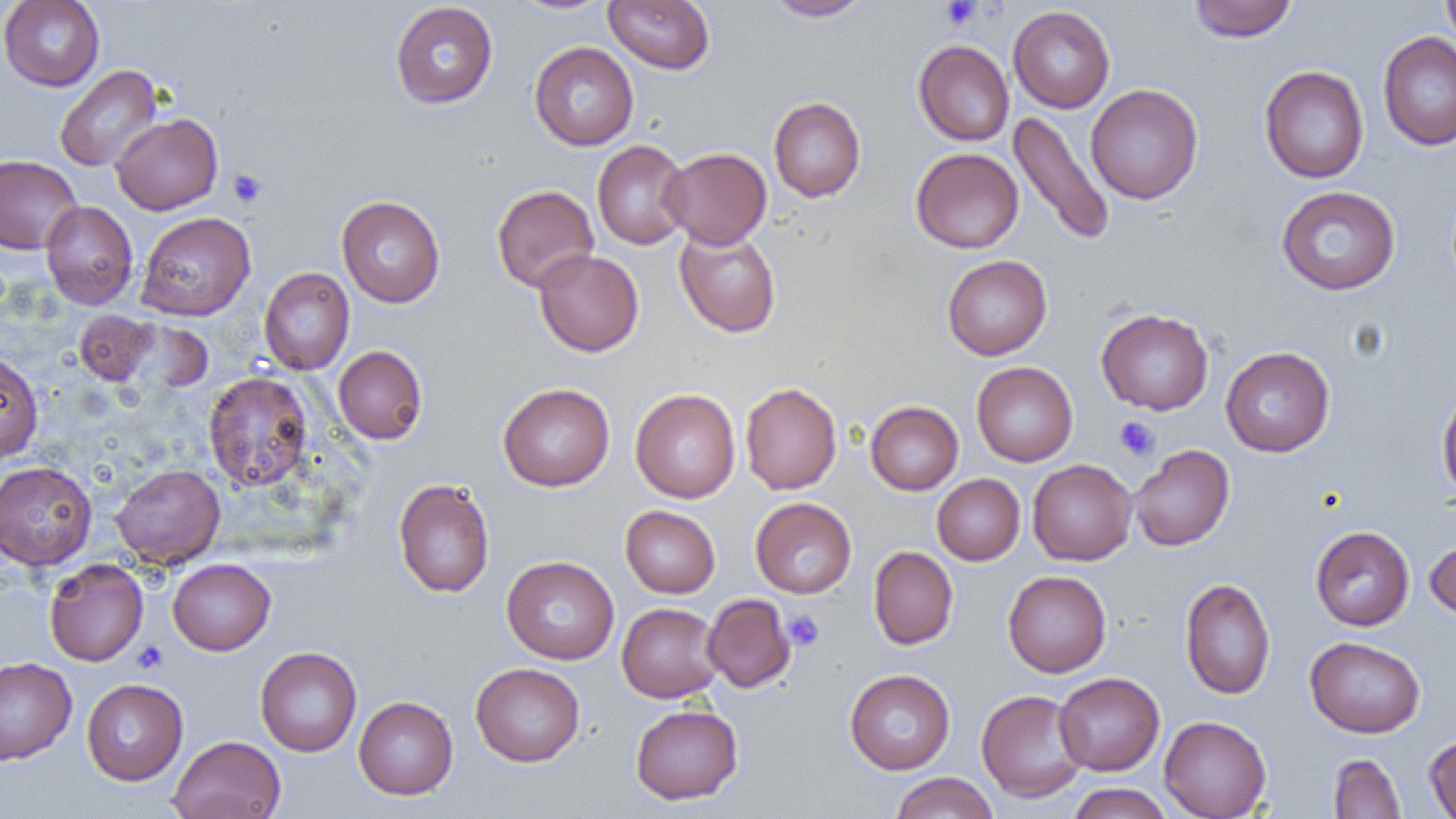

{
  "slide_level_diagnosis": "negative for blood parasites",
  "platelet_locations": "approximate bounding boxes as named x1/y1/x2/y2 corners in pixels: (x1=940, y1=0, x2=981, y2=29), (x1=228, y1=169, x2=267, y2=210), (x1=1114, y1=416, x2=1160, y2=461), (x1=783, y1=610, x2=824, y2=651), (x1=132, y1=641, x2=168, y2=673)",
  "field_of_view": "single",
  "uninfected_red_blood_cell_locations": "approximate bounding boxes as named x1/y1/x2/y2 corners in pixels: (x1=0, y1=0, x2=105, y2=91), (x1=509, y1=0, x2=616, y2=15), (x1=603, y1=0, x2=715, y2=74), (x1=764, y1=0, x2=873, y2=21), (x1=1188, y1=0, x2=1297, y2=42), (x1=1441, y1=0, x2=1456, y2=52), (x1=389, y1=2, x2=498, y2=108), (x1=1008, y1=6, x2=1115, y2=113), (x1=1378, y1=31, x2=1456, y2=150), (x1=913, y1=40, x2=1014, y2=146), (x1=529, y1=41, x2=639, y2=150), (x1=54, y1=65, x2=162, y2=172), (x1=1260, y1=65, x2=1369, y2=183), (x1=1085, y1=84, x2=1203, y2=204), (x1=769, y1=96, x2=865, y2=202), (x1=1008, y1=111, x2=1116, y2=247), (x1=111, y1=113, x2=222, y2=215), (x1=592, y1=140, x2=692, y2=250), (x1=661, y1=147, x2=772, y2=249), (x1=911, y1=148, x2=1024, y2=253), (x1=0, y1=154, x2=83, y2=254), (x1=492, y1=184, x2=599, y2=293), (x1=1276, y1=186, x2=1400, y2=295), (x1=336, y1=195, x2=446, y2=307), (x1=40, y1=201, x2=138, y2=309), (x1=135, y1=212, x2=256, y2=321), (x1=674, y1=225, x2=781, y2=338), (x1=533, y1=249, x2=644, y2=357), (x1=942, y1=255, x2=1052, y2=360), (x1=258, y1=267, x2=355, y2=375), (x1=1096, y1=308, x2=1213, y2=415), (x1=74, y1=310, x2=157, y2=385), (x1=333, y1=345, x2=428, y2=444), (x1=1221, y1=347, x2=1335, y2=457), (x1=0, y1=350, x2=43, y2=462), (x1=972, y1=362, x2=1078, y2=466), (x1=203, y1=372, x2=313, y2=491), (x1=740, y1=382, x2=842, y2=494), (x1=498, y1=383, x2=615, y2=491), (x1=1437, y1=385, x2=1456, y2=503), (x1=630, y1=388, x2=740, y2=503), (x1=865, y1=401, x2=964, y2=495), (x1=1129, y1=444, x2=1235, y2=551), (x1=1027, y1=459, x2=1137, y2=565), (x1=0, y1=461, x2=97, y2=571), (x1=110, y1=464, x2=225, y2=567), (x1=932, y1=474, x2=1024, y2=565), (x1=393, y1=478, x2=495, y2=597), (x1=751, y1=497, x2=857, y2=598), (x1=620, y1=505, x2=720, y2=598), (x1=1310, y1=525, x2=1415, y2=631), (x1=1424, y1=536, x2=1456, y2=621), (x1=868, y1=546, x2=958, y2=649), (x1=501, y1=555, x2=619, y2=664), (x1=168, y1=558, x2=275, y2=655), (x1=44, y1=559, x2=148, y2=666), (x1=1003, y1=570, x2=1111, y2=677), (x1=1180, y1=577, x2=1276, y2=700), (x1=703, y1=593, x2=796, y2=692), (x1=617, y1=602, x2=725, y2=702), (x1=1305, y1=636, x2=1425, y2=738), (x1=255, y1=646, x2=362, y2=756), (x1=0, y1=656, x2=77, y2=766), (x1=471, y1=662, x2=585, y2=766), (x1=845, y1=669, x2=955, y2=774), (x1=1054, y1=672, x2=1165, y2=775), (x1=81, y1=678, x2=188, y2=785), (x1=976, y1=689, x2=1089, y2=803), (x1=353, y1=695, x2=458, y2=800), (x1=630, y1=704, x2=743, y2=805), (x1=1159, y1=715, x2=1271, y2=819), (x1=1424, y1=733, x2=1456, y2=819), (x1=168, y1=735, x2=285, y2=819), (x1=1328, y1=754, x2=1406, y2=818), (x1=889, y1=772, x2=999, y2=818), (x1=1066, y1=783, x2=1174, y2=819)",
  "preparation": "thin blood film",
  "image_size": "1456×819 pixels",
  "magnification": "1000x",
  "modality": "light microscopy"
}